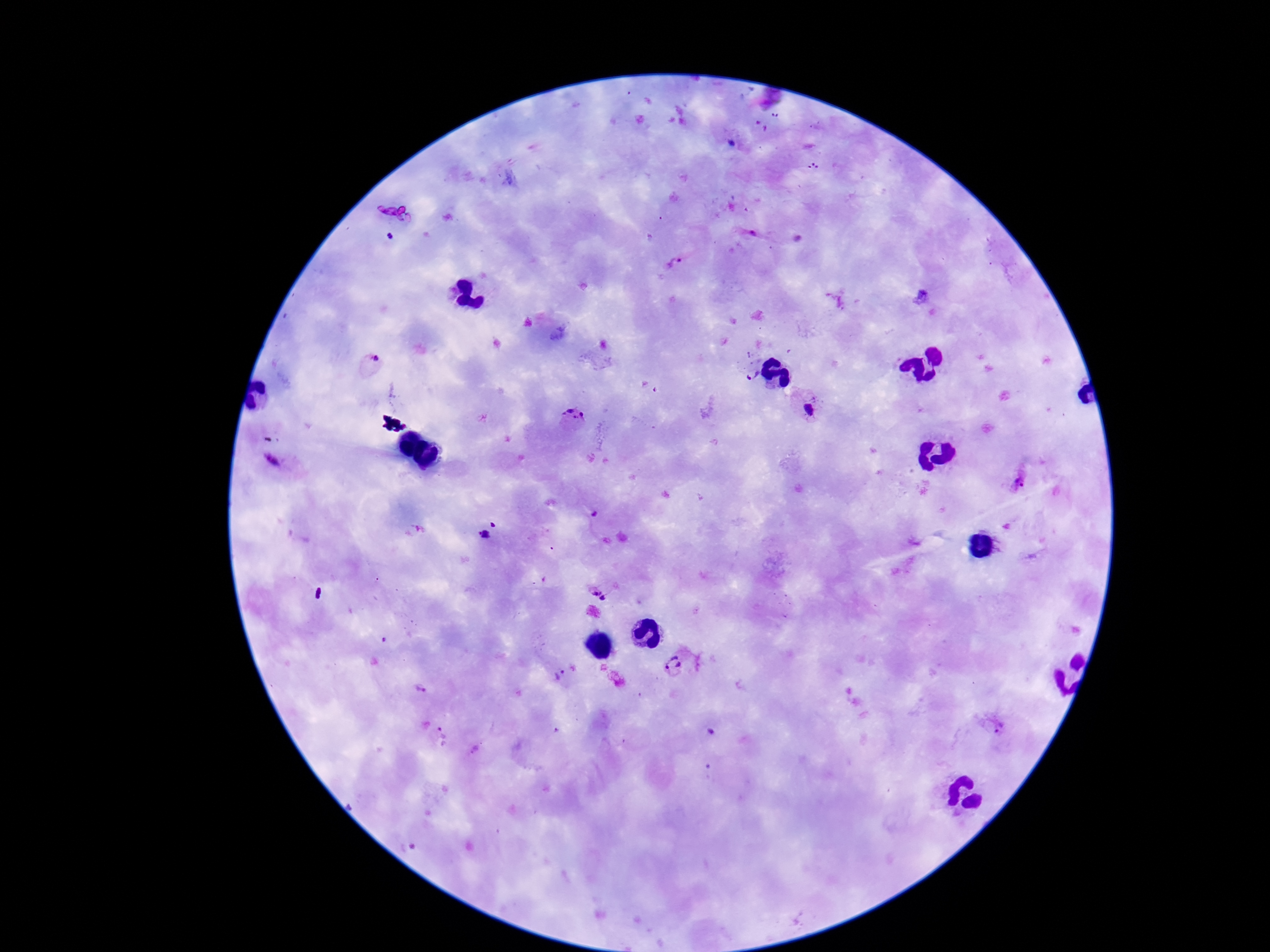
patient_malaria_status: infected
stain: Giemsa
field_of_view: single
plasmodium_parasite_locations: 'approximate centers as (x, y) in pixels: (752, 235), (390, 237), (675, 264), (374, 360), (750, 375), (809, 409), (573, 418), (272, 462), (1020, 481), (594, 515), (486, 536), (594, 590), (605, 599), (673, 665), (558, 677), (420, 689), (711, 732), (1004, 732), (444, 737)'
capture: smartphone camera through the microscope eyepiece
magnification: 100x
preparation: thick peripheral-blood smear
image_size: 1270×952 pixels